Name the blood parasite species.
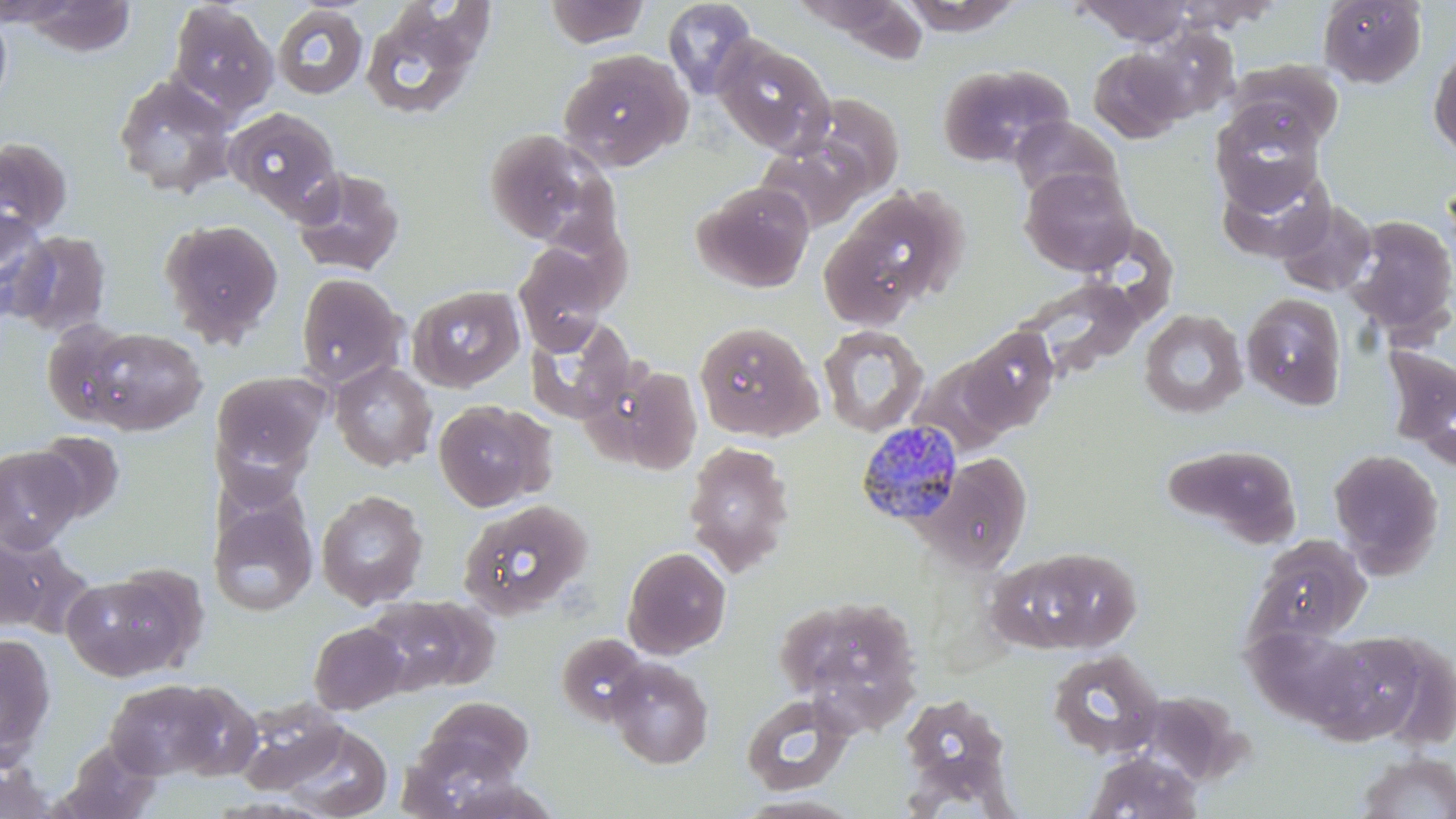

Plasmodium malariae.

Approximate bounding boxes as (x1, y1, x2, y2) in pixels. Uninfected red blood cell locations: (544, 0, 652, 48), (661, 0, 758, 98), (898, 0, 1026, 36), (1165, 0, 1284, 32), (1317, 0, 1427, 88), (1074, 1, 1199, 44), (166, 2, 279, 117), (358, 2, 495, 121), (271, 5, 368, 100), (0, 8, 13, 112), (712, 35, 835, 156), (1428, 42, 1456, 161), (1087, 47, 1191, 143), (558, 50, 691, 170), (1225, 60, 1344, 152), (937, 63, 1071, 167), (112, 75, 237, 198), (807, 93, 905, 194), (223, 106, 344, 219), (1211, 106, 1326, 211), (1009, 115, 1122, 204), (482, 129, 609, 245), (0, 136, 73, 239), (755, 137, 874, 234), (1, 138, 88, 336), (1217, 163, 1336, 262), (1020, 166, 1138, 275), (291, 167, 406, 277), (693, 180, 815, 292), (818, 190, 957, 328), (1273, 198, 1378, 297), (0, 209, 56, 323), (1344, 215, 1456, 337), (159, 218, 284, 345), (8, 229, 112, 337), (514, 244, 610, 355), (295, 272, 407, 389), (1017, 278, 1146, 380), (408, 284, 525, 392), (1241, 293, 1348, 410), (1139, 309, 1247, 419), (524, 316, 636, 424), (694, 321, 823, 441), (41, 322, 139, 427), (817, 325, 928, 437), (79, 326, 207, 435), (959, 326, 1061, 433), (1382, 344, 1456, 463), (330, 361, 437, 471), (606, 362, 704, 474), (211, 370, 329, 475), (433, 399, 552, 512), (31, 430, 125, 523), (683, 442, 796, 577), (1161, 442, 1303, 548), (0, 446, 83, 553), (1328, 449, 1443, 574), (923, 453, 1034, 573), (316, 490, 428, 609), (458, 499, 593, 619), (209, 500, 318, 616), (1248, 533, 1372, 644), (0, 536, 89, 638), (995, 545, 1144, 654), (622, 546, 731, 659), (61, 574, 191, 682), (775, 592, 923, 723), (363, 595, 489, 695), (308, 622, 407, 714), (1313, 630, 1443, 747), (0, 633, 56, 760), (556, 633, 650, 725), (1046, 651, 1165, 759), (606, 658, 714, 769), (102, 678, 231, 781), (165, 681, 263, 780), (740, 693, 855, 794), (899, 693, 1012, 792), (233, 696, 348, 793), (420, 696, 534, 784), (277, 722, 392, 819), (55, 739, 164, 819), (1080, 750, 1205, 819), (1355, 751, 1455, 818), (1, 756, 58, 817), (731, 794, 866, 818). Plasmodium malariae-infected red blood cell locations: (855, 420, 965, 528). Image is 1456×819 pixels. Optical microscopy. Thin blood film. One field of a larger specimen. May-Grünwald-Giemsa-stained preparation. Captured at 1000x magnification.